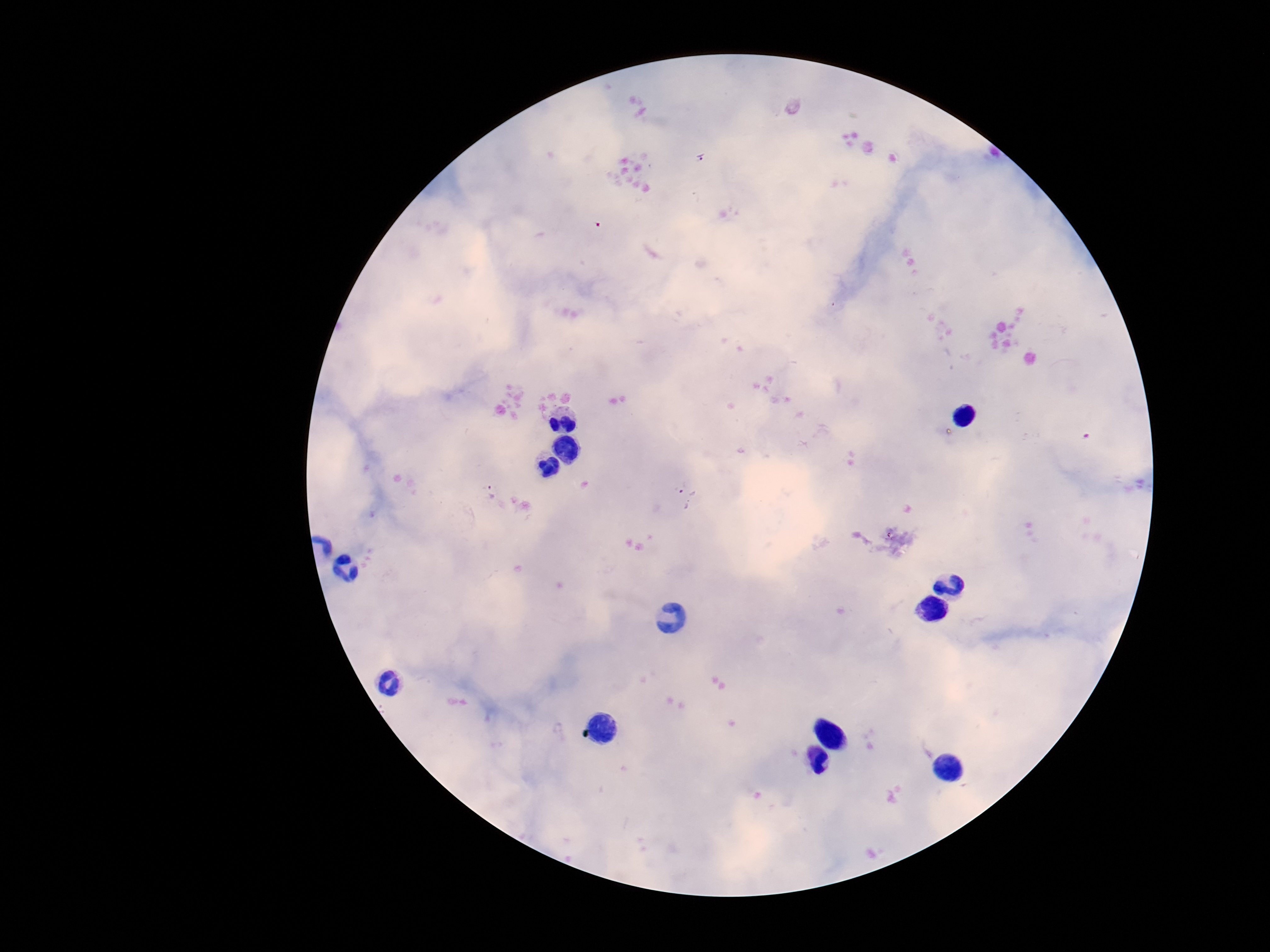

stain = Giemsa
magnification = 100x
capture = smartphone camera through the microscope eyepiece
patient malaria status = infected
field of view = one from this slide
image size = 1270×952 pixels
preparation = thick peripheral-blood smear
Plasmodium parasite locations = approximate object centers, in pixels from the top-left corner: (x=701, y=157), (x=492, y=492), (x=688, y=497)